Name the parasite shown.
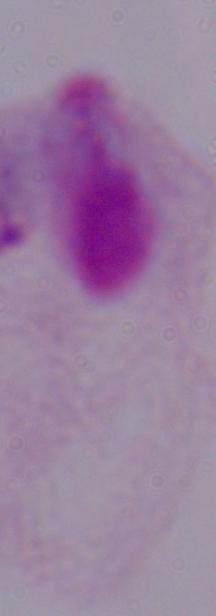
This is a trichomonad.

Micrograph. Captured at 1000x magnification.